Point out every Plasmodium parasite and every leukocyte.
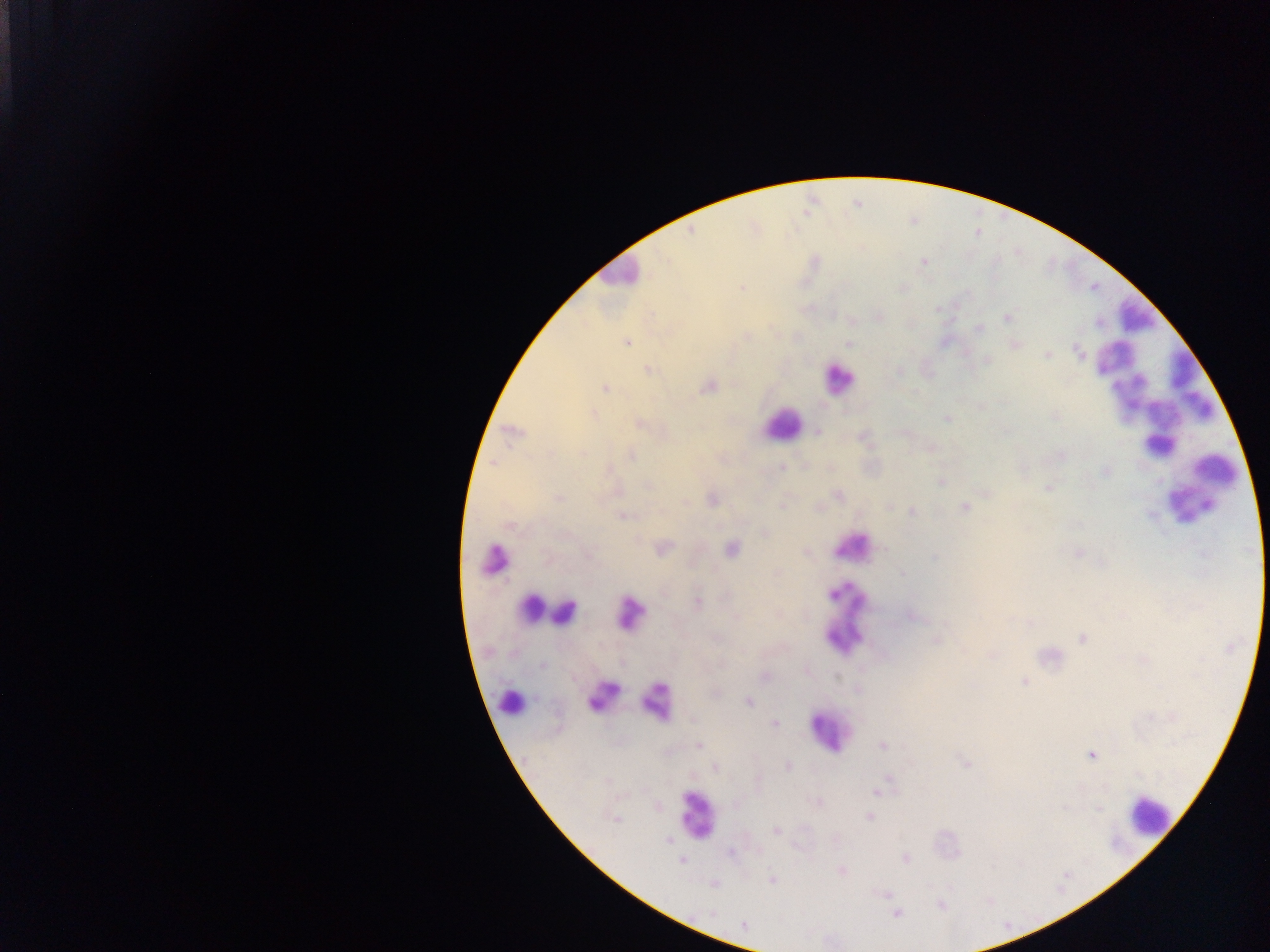

Approximate centers as (x, y) in pixels.
Plasmodium parasites: (740, 288), (1006, 317), (979, 330), (746, 337), (627, 342), (848, 344), (1015, 346), (1081, 353), (1047, 355), (988, 362), (647, 369), (708, 386), (607, 387), (593, 414), (1055, 415), (946, 418), (640, 424), (818, 432), (630, 454), (1065, 454), (781, 466), (1106, 471), (941, 483), (1048, 487), (839, 494), (988, 494), (560, 497), (712, 500), (782, 504), (964, 506), (911, 510), (621, 516), (732, 549), (660, 551), (805, 551), (1077, 552), (901, 575), (699, 605), (912, 616), (1032, 624), (1081, 637), (937, 640), (543, 665), (837, 678), (1024, 681), (749, 702), (775, 724), (699, 745), (882, 747), (1091, 755), (788, 766), (715, 768), (890, 778), (877, 792), (1099, 808), (869, 817), (776, 830), (755, 853), (732, 854), (905, 859), (842, 871), (771, 879), (887, 894), (940, 904), (896, 914).
Leukocytes: (1123, 324), (1111, 363), (831, 381), (1172, 407), (774, 426), (1185, 509), (849, 550), (492, 561), (548, 612), (848, 620), (602, 698), (509, 700), (659, 702), (829, 731), (690, 813), (1152, 815).

{
  "capture": "mobile-phone photograph through a microscope",
  "field_of_view": "single",
  "image_size": "1270×952 pixels",
  "preparation": "thick blood film",
  "country": "Ghana"
}